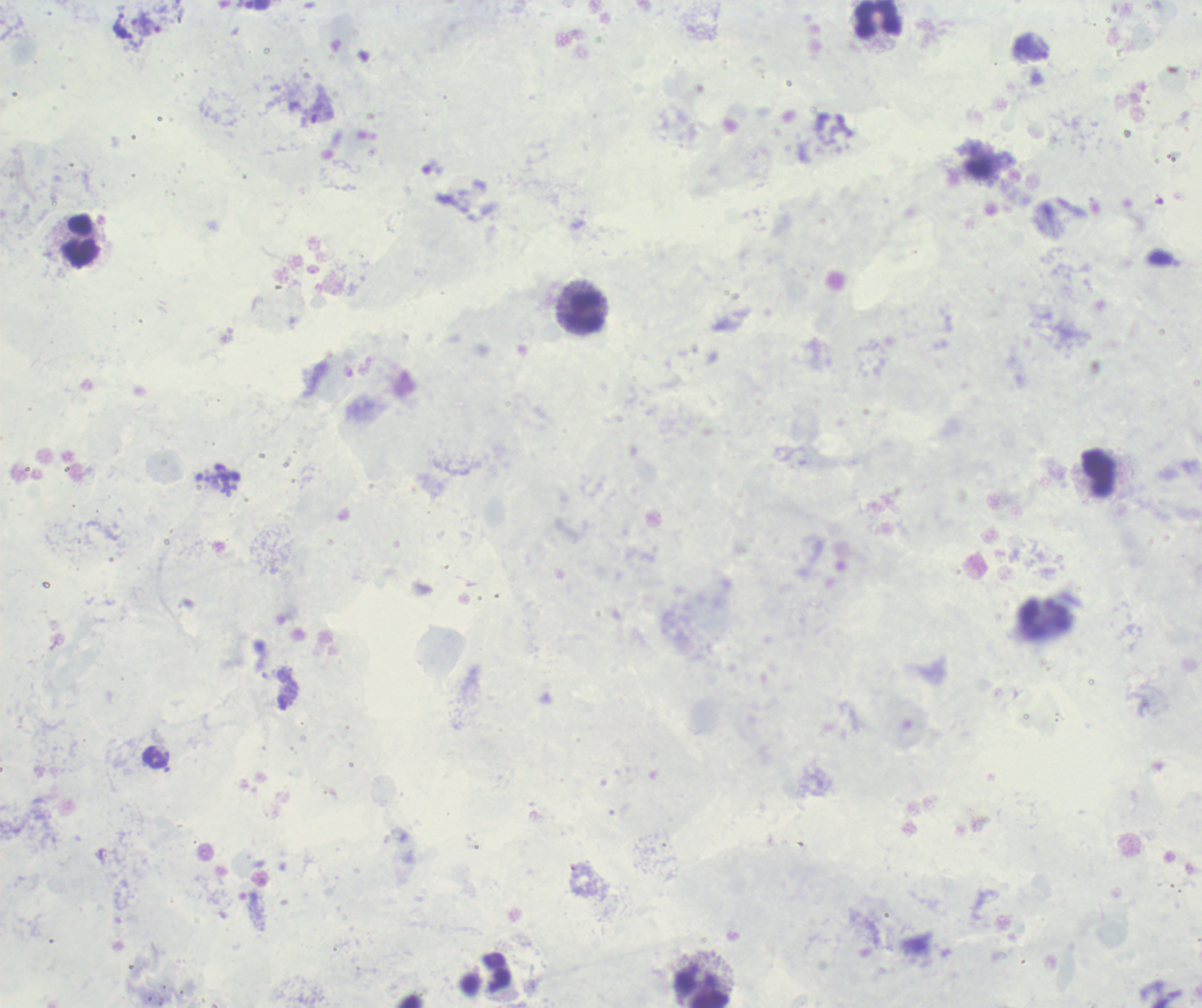
background_quality: poor
magnification: 100x
field_of_view: one from this slide
preparation: thick blood film
trophozoite_locations: 'approximate centers as (x, y) in pixels: (125, 34), (321, 112)'
stain: Romanowsky
result: positive for malaria parasites
leukocyte_locations: 'approximate centers as (x, y) in pixels: (879, 19), (81, 240), (584, 310), (1098, 473), (1045, 619), (701, 989)'
context: previously used in a real diagnosis
image_size: 1202×1008 pixels